Identify the parasite.
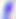
Toxoplasma gondii.

{
  "modality": "photomicrograph",
  "magnification": "400x"
}